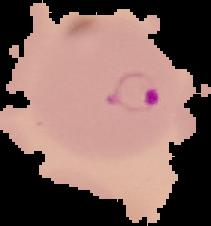

preparation = thin blood film
image type = segmented cell region on a black background
malaria status = parasitized
image size = 211×226 pixels